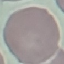

malaria_status: uninfected
preparation: thin blood smear
image_type: automatically extracted cell patch, resized to 64 × 64 pixels
capture: smartphone through the microscope eyepiece
stain: Giemsa